Classify this cell by malaria status.
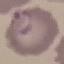

Parasitized.

Automatically extracted cell patch, resized to 64 × 64 pixels. Photographed with a smartphone camera at the microscope eyepiece. Thin blood smear. Giemsa stain.